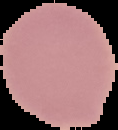
result = no Plasmodium parasites detected
image type = segmented cell region on a black background
preparation = thin blood smear
image size = 118×130 pixels